State which parasite is depicted.
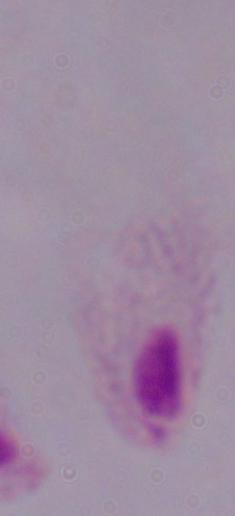

A trichomonad.

Summary:
  - Magnification: 1000x
  - Modality: micrograph